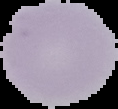

Image is 118×109 pixels. Malaria status: uninfected. From a thin blood smear. Segmented cell region on a black background.